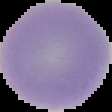 The area outside the segmented cell region is set to black. Result: no malaria parasites seen. From a thin blood smear. Image is 112×112 pixels.